Assess for malaria.
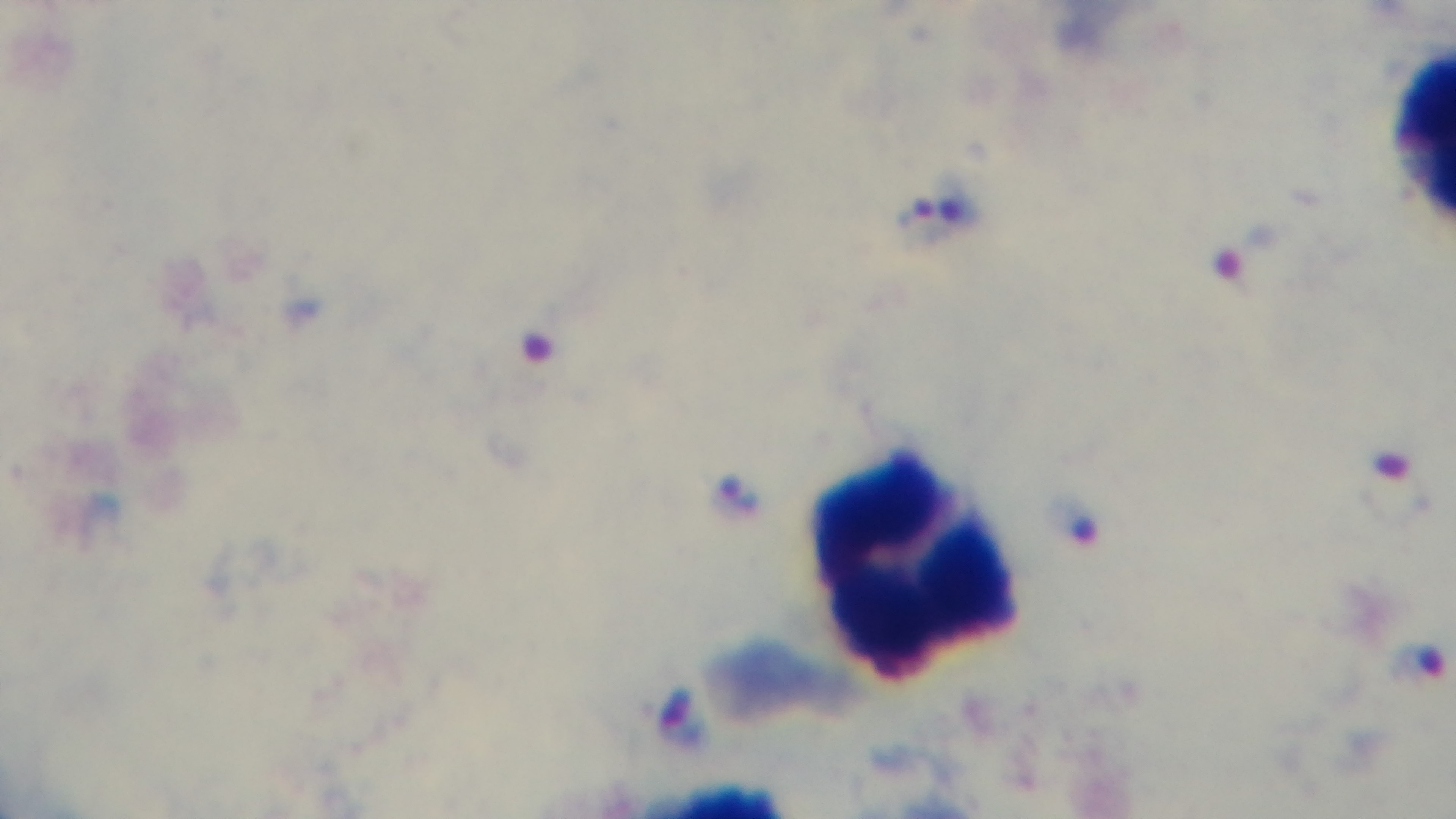
Infected.

preparation = thick blood film
modality = light microscopy
objective = 100x oil immersion
field of view = single
capture = mounted 4K digital camera
stain = Giemsa